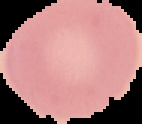
Summary:
  - Image size: 142×124 pixels
  - Preparation: thin blood film
  - Malaria status: uninfected
  - Image type: cell region segmented out of the field of view; surrounding area masked to black